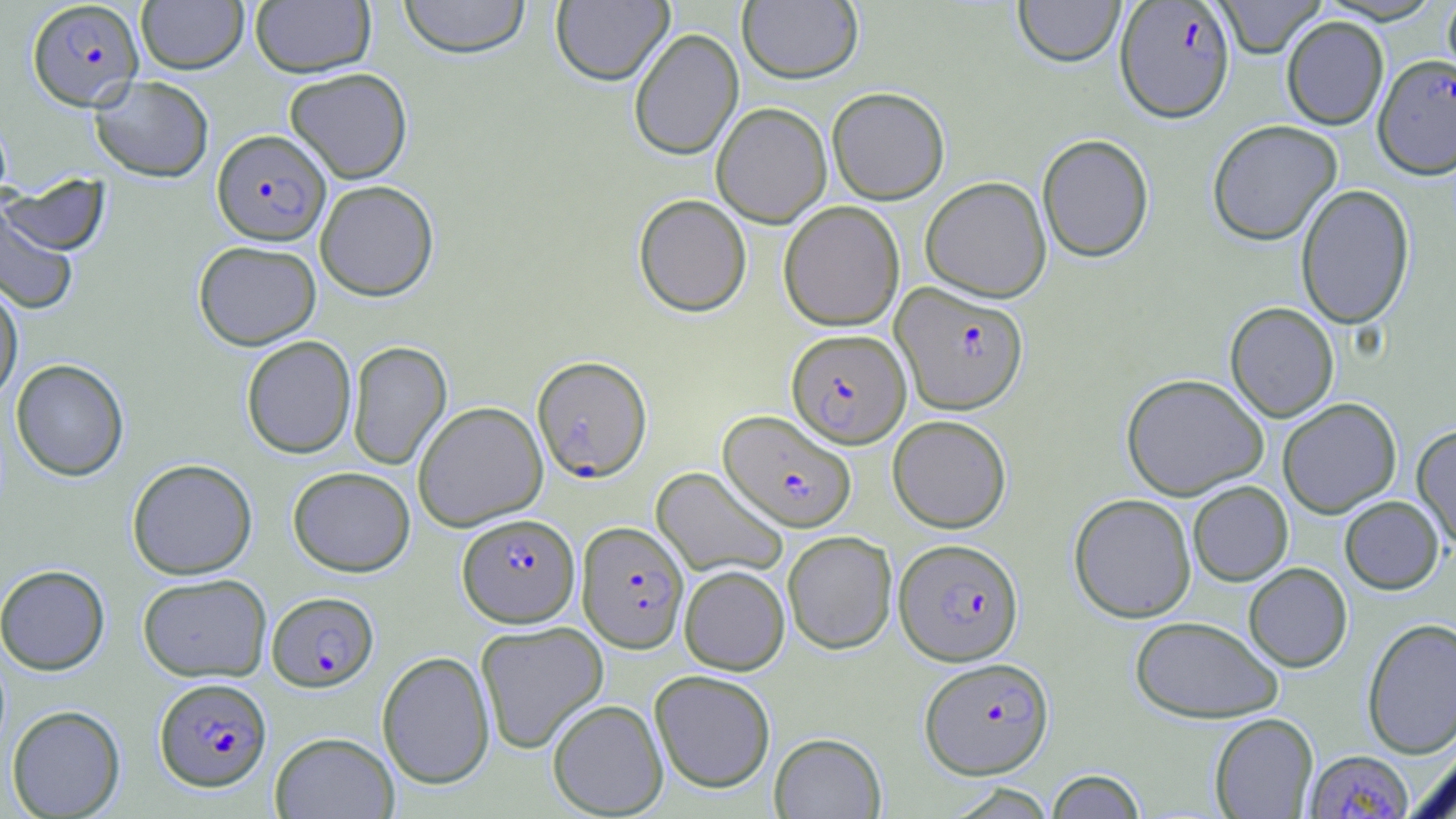 Approximate bounding boxes as [x1, y1, x2, y2] in pixels. Plasmodium falciparum-infected red blood cell locations: [26, 0, 144, 110], [1115, 1, 1235, 122], [1373, 54, 1456, 179], [212, 129, 330, 245], [891, 282, 1028, 415], [788, 333, 912, 452], [532, 355, 652, 482], [719, 409, 857, 531], [457, 513, 579, 627], [576, 521, 689, 653], [894, 538, 1023, 665], [267, 591, 379, 691], [919, 657, 1055, 779], [154, 677, 272, 791], [1305, 749, 1413, 818]. Uninfected red blood cell locations: [137, 0, 248, 74], [398, 0, 532, 59], [551, 0, 673, 85], [738, 0, 863, 84], [1013, 0, 1125, 66], [1212, 0, 1327, 58], [1442, 0, 1456, 86], [250, 1, 375, 77], [1281, 16, 1388, 130], [628, 28, 743, 160], [284, 67, 413, 183], [89, 75, 214, 182], [827, 86, 950, 204], [711, 102, 832, 227], [1207, 119, 1342, 245], [1037, 133, 1154, 262], [2, 174, 111, 256], [920, 176, 1051, 302], [315, 180, 439, 301], [1296, 183, 1415, 329], [633, 193, 752, 316], [0, 200, 80, 315], [779, 200, 905, 331], [193, 240, 321, 350], [0, 278, 23, 405], [1225, 302, 1339, 421], [241, 335, 357, 458], [347, 341, 452, 470], [11, 358, 129, 481], [1121, 372, 1269, 500], [1278, 398, 1401, 518], [412, 400, 548, 531], [888, 415, 1012, 533], [1412, 424, 1456, 550], [127, 458, 257, 579], [288, 466, 415, 576], [651, 466, 788, 579], [1188, 481, 1293, 585], [1069, 493, 1196, 623], [1340, 496, 1444, 594], [782, 531, 897, 654], [1244, 563, 1352, 671], [0, 564, 110, 675], [679, 565, 789, 675], [137, 573, 272, 682], [1130, 616, 1284, 723], [1362, 617, 1456, 758], [475, 621, 608, 752], [377, 650, 495, 789], [650, 669, 776, 793], [547, 699, 668, 817], [6, 704, 126, 818], [1209, 713, 1318, 818], [270, 731, 399, 818], [770, 732, 886, 818], [1410, 743, 1456, 818], [1045, 770, 1146, 818]. Slide-level diagnosis: Plasmodium falciparum. Light microscopy. Image is 1456×819 pixels. One field of a larger specimen. May-Grünwald-Giemsa-stained preparation. 1000x magnification. Thin blood smear.